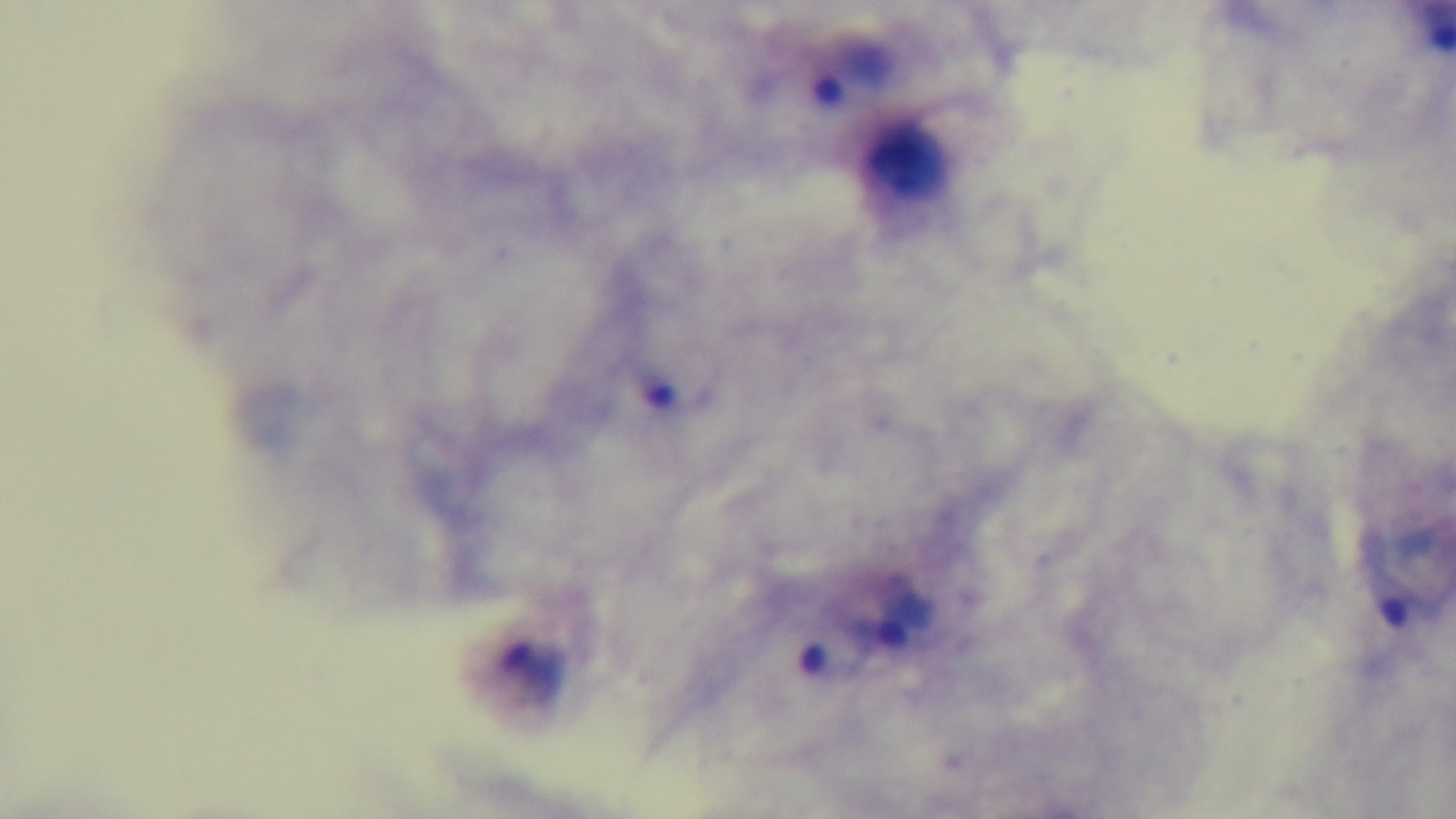
Summary:
  - Modality: light microscopy
  - Preparation: thick
  - Objective: 100x oil immersion
  - Field of view: single
  - Stain: Giemsa
  - Malaria status: infected
  - Capture: mounted 4K digital camera